Assess this cell for malaria.
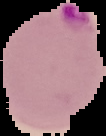
It is parasitized.

preparation = thin blood film
image type = cell region segmented out of the field of view; surrounding area masked to black
image size = 106×136 pixels